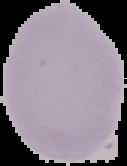
Summary:
  - Image type: segmented cell region on a black background
  - Preparation: thin blood smear
  - Image size: 127×166 pixels
  - Malaria status: uninfected